Report the malaria status of this cell.
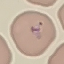

Parasitized.

Summary:
  - Image type: cell patch, automatically extracted from a larger field of view and resized to 64 × 64 pixels
  - Stain: Giemsa
  - Preparation: thin smear
  - Capture: smartphone camera at the microscope eyepiece